Locate and identify every blood parasite.
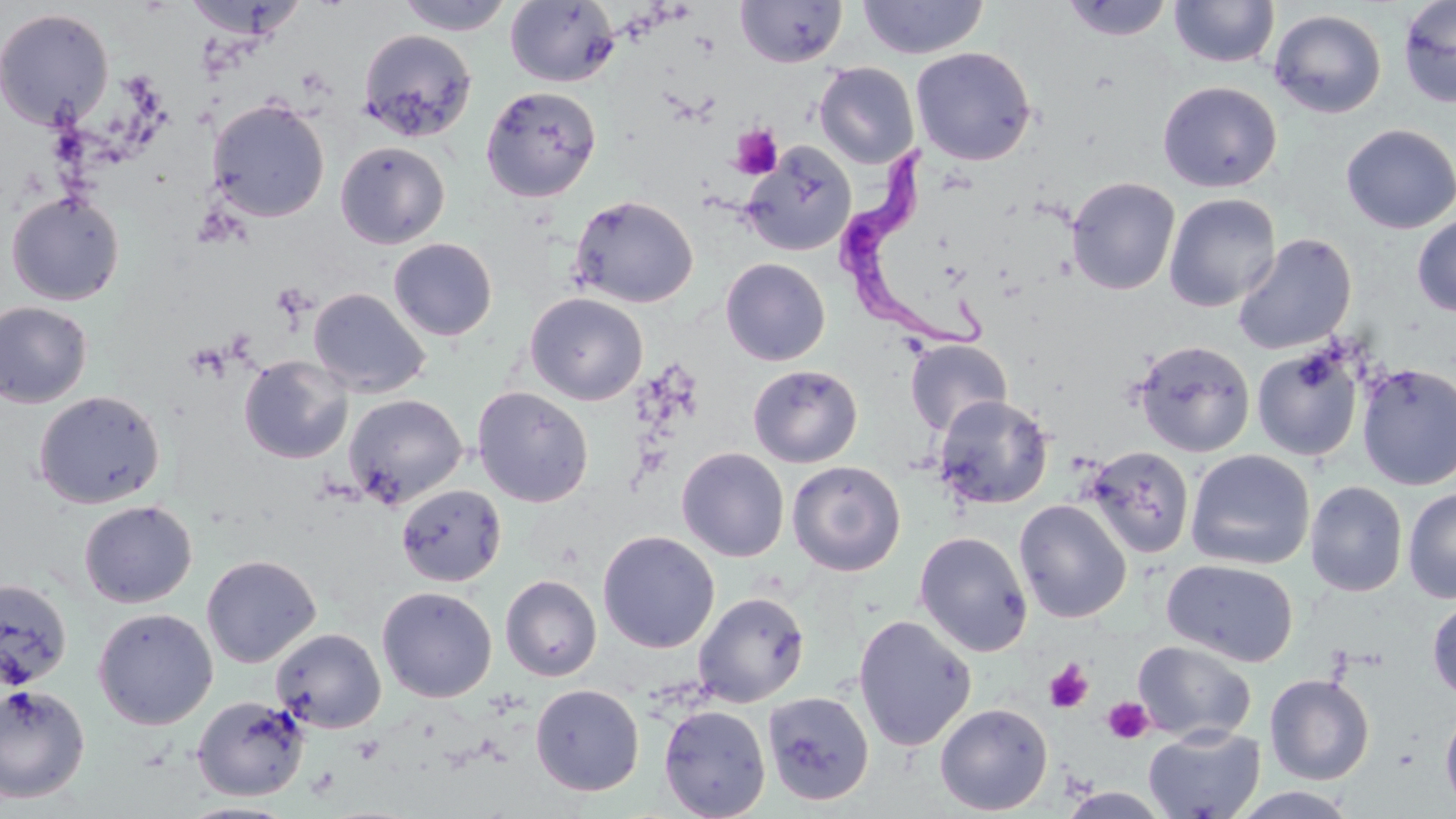
Approximate bounding boxes as (x1, y1, x2, y2) in pixels.
Trypanosoma brucei: (835, 148, 996, 355).
No Plasmodium falciparum, Plasmodium ovale, Plasmodium malariae, Plasmodium vivax, or Babesia divergens observed.

{
  "slide_level_diagnosis": "Trypanosoma brucei",
  "preparation": "thin blood smear",
  "platelet_locations": "approximate bounding boxes as (x1, y1, x2, y2) in pixels: (730, 125, 783, 179), (185, 343, 230, 383), (1044, 659, 1094, 714), (1103, 695, 1154, 744)",
  "magnification": "1000x",
  "field_of_view": "one of a larger specimen",
  "uninfected_red_blood_cell_locations": "approximate bounding boxes as (x1, y1, x2, y2) in pixels: (181, 0, 304, 40), (394, 0, 515, 35), (505, 0, 620, 87), (857, 0, 988, 59), (1061, 0, 1174, 41), (1398, 0, 1456, 108), (735, 1, 848, 68), (1169, 1, 1280, 68), (0, 8, 115, 131), (1268, 9, 1387, 119), (358, 28, 478, 142), (910, 46, 1037, 165), (814, 62, 919, 168), (1157, 81, 1282, 193), (480, 86, 602, 202), (208, 98, 330, 222), (1340, 124, 1456, 233), (335, 140, 450, 249), (740, 143, 856, 256), (1066, 176, 1180, 295), (6, 191, 125, 306), (569, 193, 699, 308), (1163, 193, 1281, 312), (1412, 213, 1456, 317), (1232, 233, 1357, 355), (388, 237, 498, 341), (720, 258, 830, 366), (308, 287, 430, 398), (525, 292, 648, 405), (0, 301, 93, 408), (905, 338, 1012, 435), (1133, 339, 1256, 457), (1251, 348, 1363, 461), (239, 355, 353, 464), (1357, 363, 1456, 491), (747, 364, 863, 468), (472, 386, 594, 507), (33, 390, 165, 509), (344, 394, 467, 508), (934, 394, 1054, 510), (1083, 445, 1195, 559), (676, 447, 789, 562), (1186, 450, 1315, 570), (787, 460, 906, 576), (1305, 480, 1407, 597), (396, 483, 507, 587), (1403, 487, 1456, 603), (1014, 499, 1131, 623), (79, 500, 197, 608), (598, 530, 720, 653), (914, 531, 1033, 656), (201, 553, 321, 668), (1162, 558, 1299, 667), (500, 574, 602, 681), (0, 577, 72, 691), (376, 586, 497, 703), (693, 591, 810, 707), (1426, 596, 1456, 703), (92, 607, 218, 730), (853, 614, 977, 751), (270, 627, 387, 733), (1133, 639, 1257, 743), (1264, 673, 1375, 785), (0, 683, 91, 803), (530, 684, 644, 796), (763, 691, 875, 806), (192, 695, 309, 801), (935, 702, 1053, 815), (1440, 702, 1456, 814), (659, 704, 771, 818), (1143, 725, 1266, 819), (1056, 787, 1174, 818), (1230, 787, 1361, 819), (178, 801, 299, 819)",
  "modality": "light microscopy",
  "image_size": "1456×819 pixels",
  "stain": "May-Grünwald-Giemsa"
}